Report the malaria status of this cell.
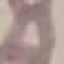
Uninfected.

Summary:
  - Image type: cell patch, automatically extracted from a larger field of view and resized to 64 × 64 pixels
  - Stain: Giemsa
  - Preparation: thin blood smear
  - Capture: smartphone through the microscope eyepiece